Locate every white blood cell.
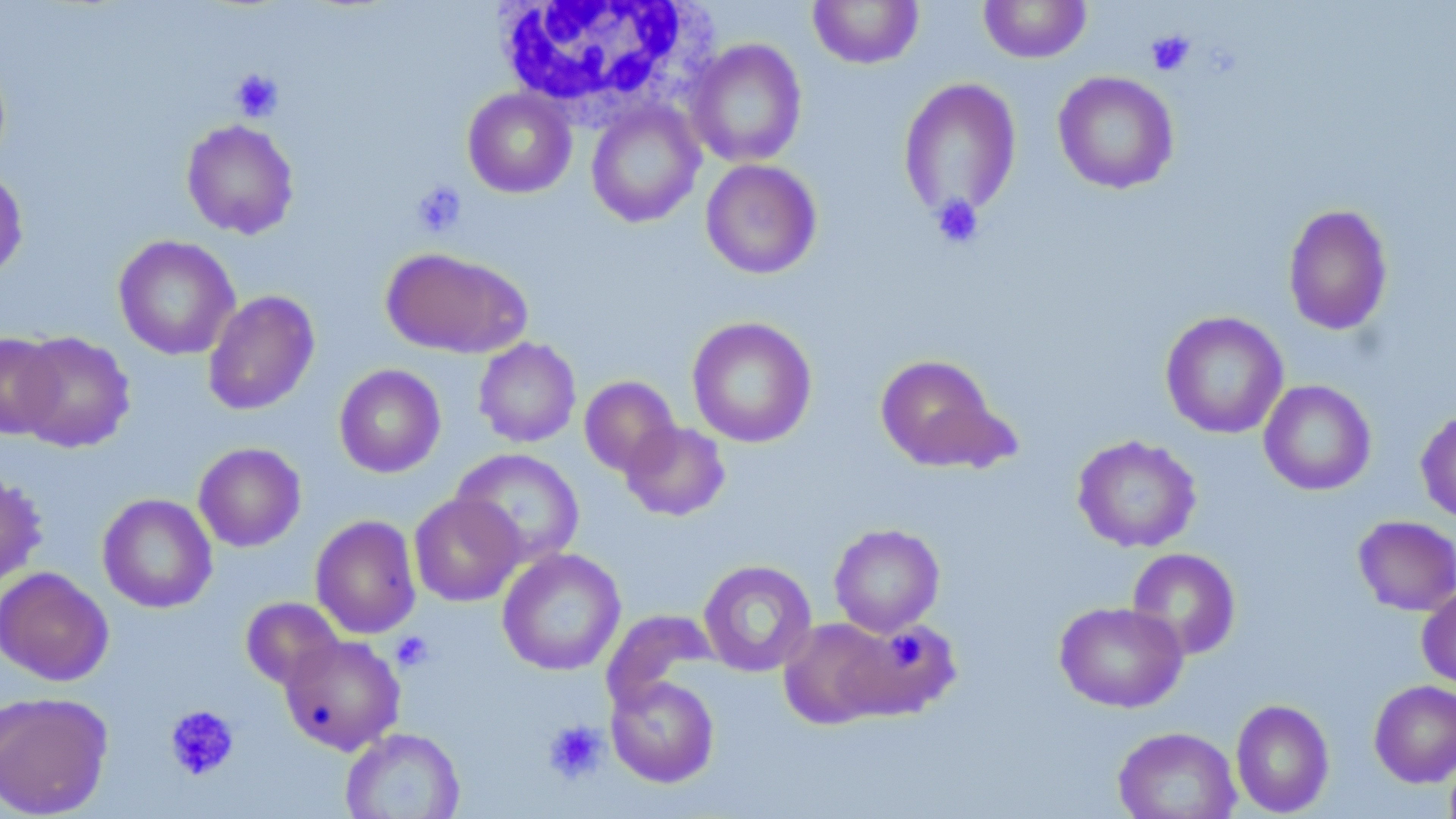
Approximate bounding boxes as [x1, y1, x2, y2] in pixels.
White blood cells: [491, 0, 712, 121].

Uninfected red blood cell locations: [808, 0, 924, 69], [979, 0, 1091, 63], [686, 38, 807, 168], [1052, 71, 1180, 194], [898, 77, 1023, 221], [462, 88, 576, 198], [586, 101, 705, 228], [181, 119, 299, 239], [701, 159, 822, 279], [0, 169, 28, 283], [1283, 204, 1394, 336], [113, 235, 239, 360], [380, 247, 531, 358], [202, 289, 320, 416], [1160, 311, 1289, 439], [686, 316, 817, 448], [14, 331, 136, 452], [0, 333, 65, 439], [473, 337, 581, 448], [874, 354, 1011, 472], [333, 363, 446, 478], [579, 375, 680, 477], [1259, 380, 1376, 496], [1415, 407, 1456, 525], [621, 421, 731, 521], [1072, 435, 1202, 553], [193, 442, 306, 552], [451, 448, 585, 567], [0, 472, 47, 589], [97, 493, 217, 613], [409, 493, 524, 607], [310, 514, 422, 639], [1352, 515, 1456, 616], [829, 523, 945, 637], [497, 548, 626, 676], [1126, 548, 1241, 660], [698, 559, 817, 677], [0, 566, 114, 686], [1417, 584, 1456, 690], [240, 597, 344, 690], [1054, 600, 1188, 713], [602, 609, 719, 709], [778, 617, 896, 729], [841, 619, 962, 720], [280, 634, 405, 754], [606, 676, 720, 787], [1369, 680, 1456, 787], [0, 690, 113, 818], [1230, 698, 1335, 816], [1112, 726, 1241, 819], [340, 727, 465, 819]. Platelet locations: [1146, 30, 1195, 76], [230, 69, 284, 121], [411, 181, 467, 238], [930, 194, 984, 249], [391, 630, 434, 671], [893, 639, 928, 670], [164, 705, 240, 780], [542, 719, 607, 783]. Slide-level diagnosis: negative for blood parasites. Light microscopy. May-Grünwald-Giemsa-stained preparation. Thin blood film. Image is 1456×819 pixels. Captured at 1000x magnification. One field of a larger specimen.